Assess this cell for malaria.
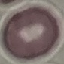

Uninfected.

{
  "preparation": "thin smear",
  "stain": "Giemsa",
  "image_type": "cell patch, automatically extracted from a larger field of view and resized to 64 × 64 pixels",
  "capture": "smartphone through the microscope eyepiece"
}